Report the malaria status of this cell.
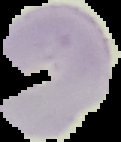
It is uninfected.

Image is 121×142 pixels. From a thin blood film. Cell region segmented out of the field of view; the surrounding area is masked to black.